Locate every blood parasite and identify its species.
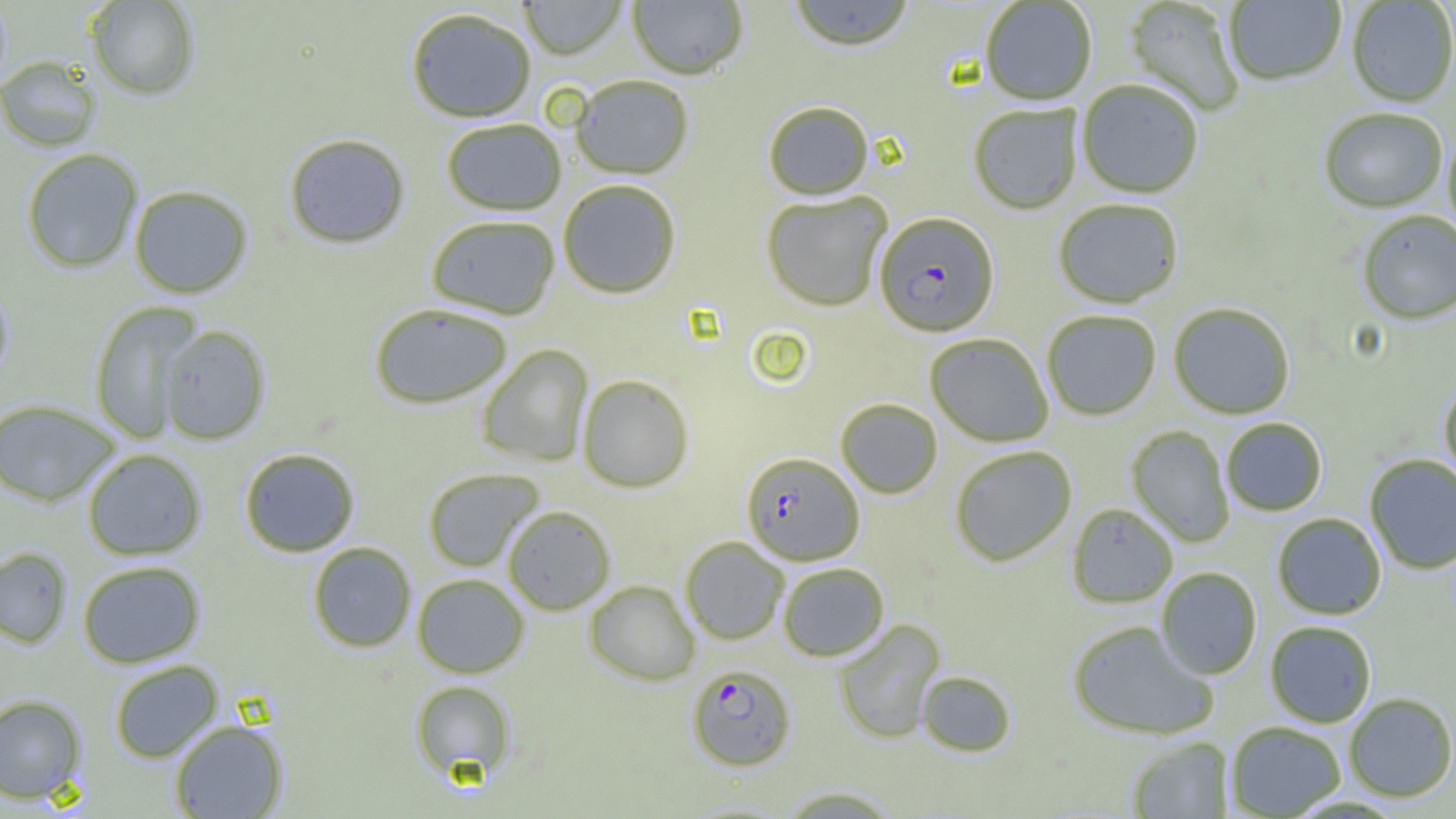

Approximate bounding boxes as [x1, y1, x2, y2] in pixels.
Plasmodium falciparum-infected red blood cells: [874, 213, 999, 338], [741, 452, 864, 566], [687, 664, 796, 771].
No Plasmodium ovale, Plasmodium malariae, Plasmodium vivax, Babesia divergens, or Trypanosoma brucei observed.

Summary:
  - Uninfected red blood cell locations: [86, 0, 201, 101], [519, 0, 627, 60], [628, 0, 748, 80], [788, 0, 914, 53], [981, 1, 1097, 106], [1123, 1, 1246, 117], [1224, 1, 1347, 87], [1347, 1, 1456, 108], [406, 8, 536, 123], [0, 57, 101, 152], [571, 76, 694, 180], [1077, 82, 1204, 199], [762, 102, 874, 201], [969, 104, 1083, 215], [1318, 109, 1447, 215], [441, 119, 567, 216], [1443, 132, 1456, 246], [284, 133, 410, 249], [21, 148, 143, 274], [558, 180, 681, 299], [128, 184, 253, 299], [761, 192, 892, 312], [1053, 200, 1184, 310], [1357, 211, 1456, 326], [426, 215, 560, 320], [0, 276, 15, 390], [89, 301, 203, 444], [370, 303, 513, 409], [1168, 303, 1295, 420], [1042, 311, 1161, 421], [157, 325, 271, 445], [938, 332, 1058, 566], [925, 334, 1053, 448], [477, 344, 593, 467], [577, 374, 694, 493], [1439, 381, 1456, 491], [0, 399, 121, 507], [835, 399, 943, 499], [1221, 418, 1327, 516], [1126, 425, 1235, 547], [950, 446, 1077, 567], [239, 447, 361, 557], [82, 449, 207, 561], [1365, 454, 1456, 575], [423, 468, 543, 572], [1067, 504, 1178, 608], [502, 505, 615, 615], [1272, 513, 1386, 620], [680, 536, 789, 645], [307, 542, 417, 653], [0, 547, 73, 649], [77, 560, 206, 668], [779, 563, 889, 662], [1156, 567, 1261, 680], [412, 574, 529, 678], [584, 580, 700, 686], [834, 619, 946, 744], [1067, 621, 1217, 741], [1265, 621, 1377, 728], [109, 660, 223, 763], [917, 671, 1016, 757], [410, 680, 516, 782], [0, 693, 87, 804], [1343, 693, 1456, 803], [168, 719, 289, 818], [1225, 721, 1346, 818], [1127, 737, 1233, 818], [776, 786, 903, 818]
  - Slide-level diagnosis: Plasmodium falciparum
  - Preparation: thin blood smear
  - Image size: 1456×819 pixels
  - Modality: optical microscopy
  - Magnification: 1000x
  - Field of view: one of a larger specimen